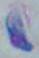

magnification = 1000x
identification = Toxoplasma gondii
modality = photomicrograph